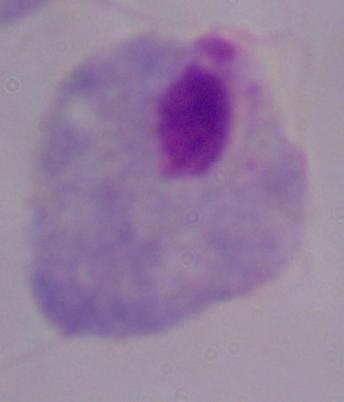

Summary:
  - Magnification: 1000x
  - Identification: trichomonad
  - Modality: micrograph